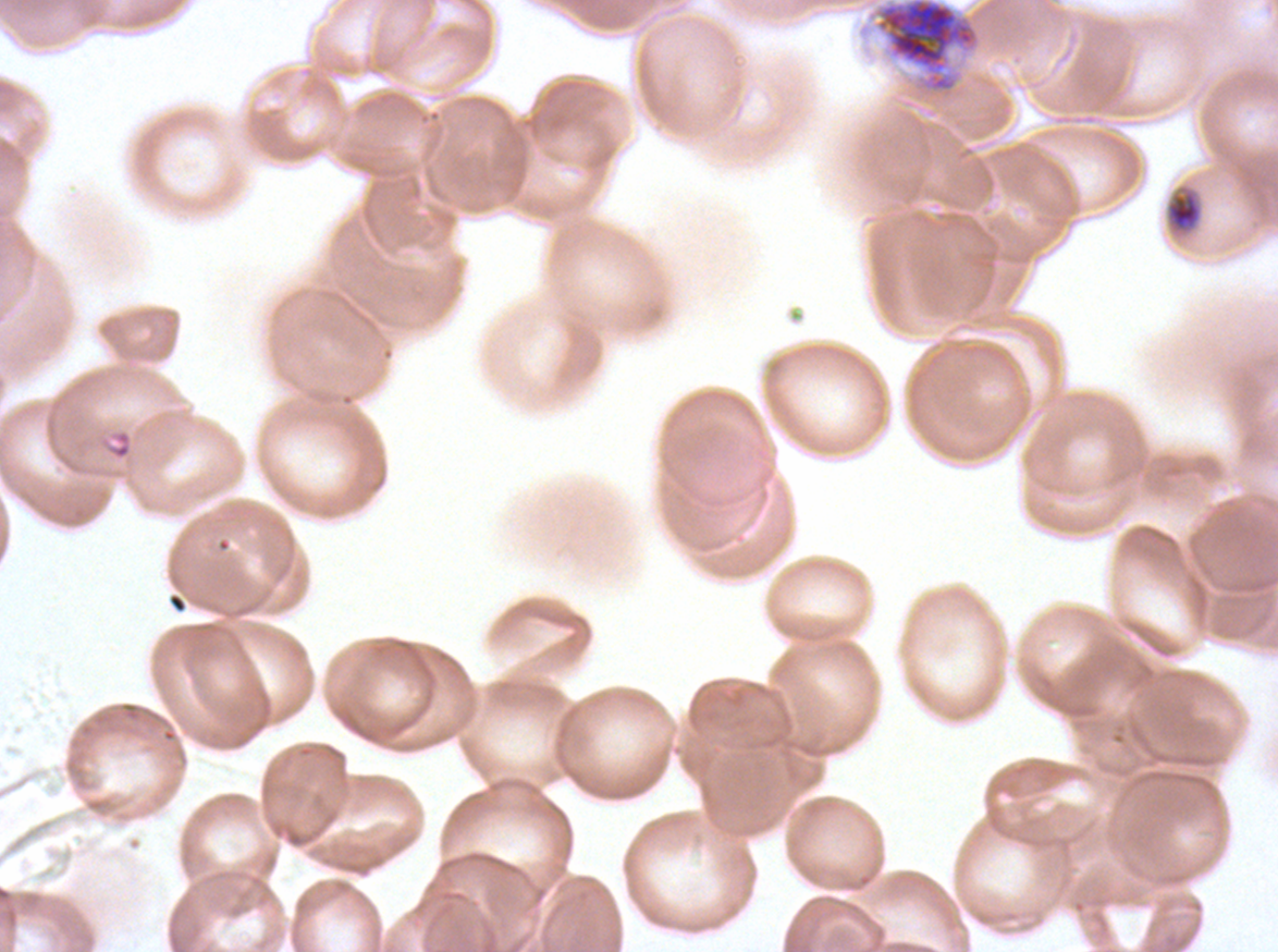
Approximate bounding boxes as (x1, y1, x2, y2) in pixels.
Summary:
  - Early schizont locations: (873, 0, 981, 94)
  - Mid trophozoite locations: (1164, 184, 1203, 236)
  - Ring locations: (99, 428, 133, 461)
  - Life-cycle stages observed: ring, mid trophozoite, early schizont
  - Image size: 1278×952 pixels
  - Stain: Giemsa
  - Specimen: ex-vivo P. falciparum culture from a patient in The Gambia, grown for 24 to 48 hours
  - Field of view: sub-image separated from a larger composite
  - Preparation: thin blood film